Assess the morphology of the erythrocytes.
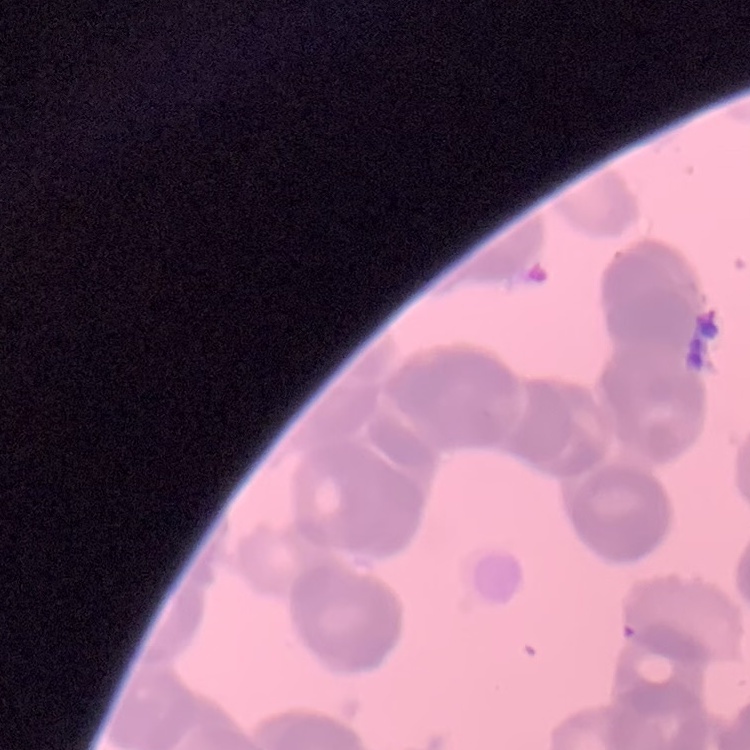

Rouleaux formation.

Thin blood film. One tile cut from a larger photomicrograph. Field's or Giemsa stain.